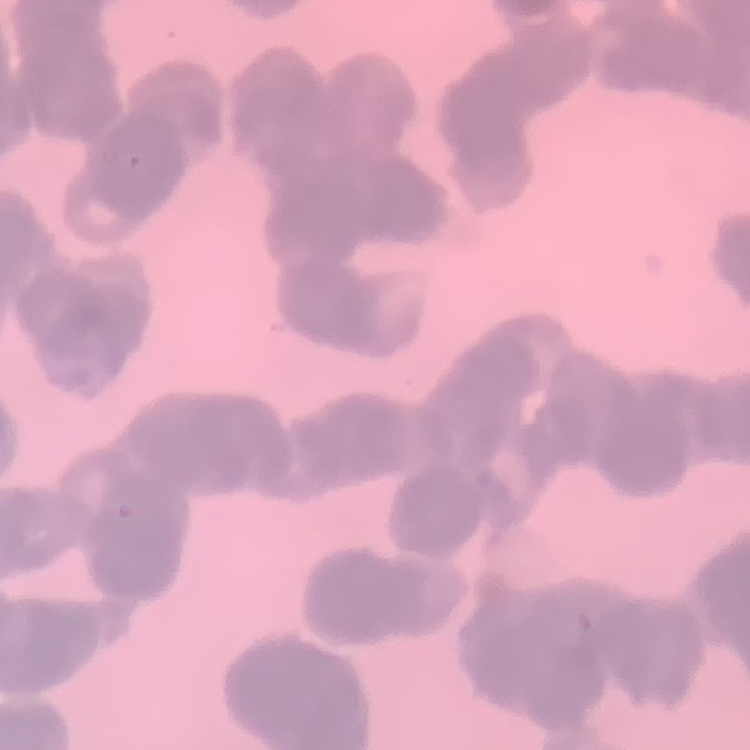
Summary:
  - Red blood cell morphology: rouleaux formation
  - Image type: one tile cut from a larger photomicrograph
  - Preparation: thin peripheral smear
  - Stain: Field's or Giemsa